Give the position of every leukocyte visible.
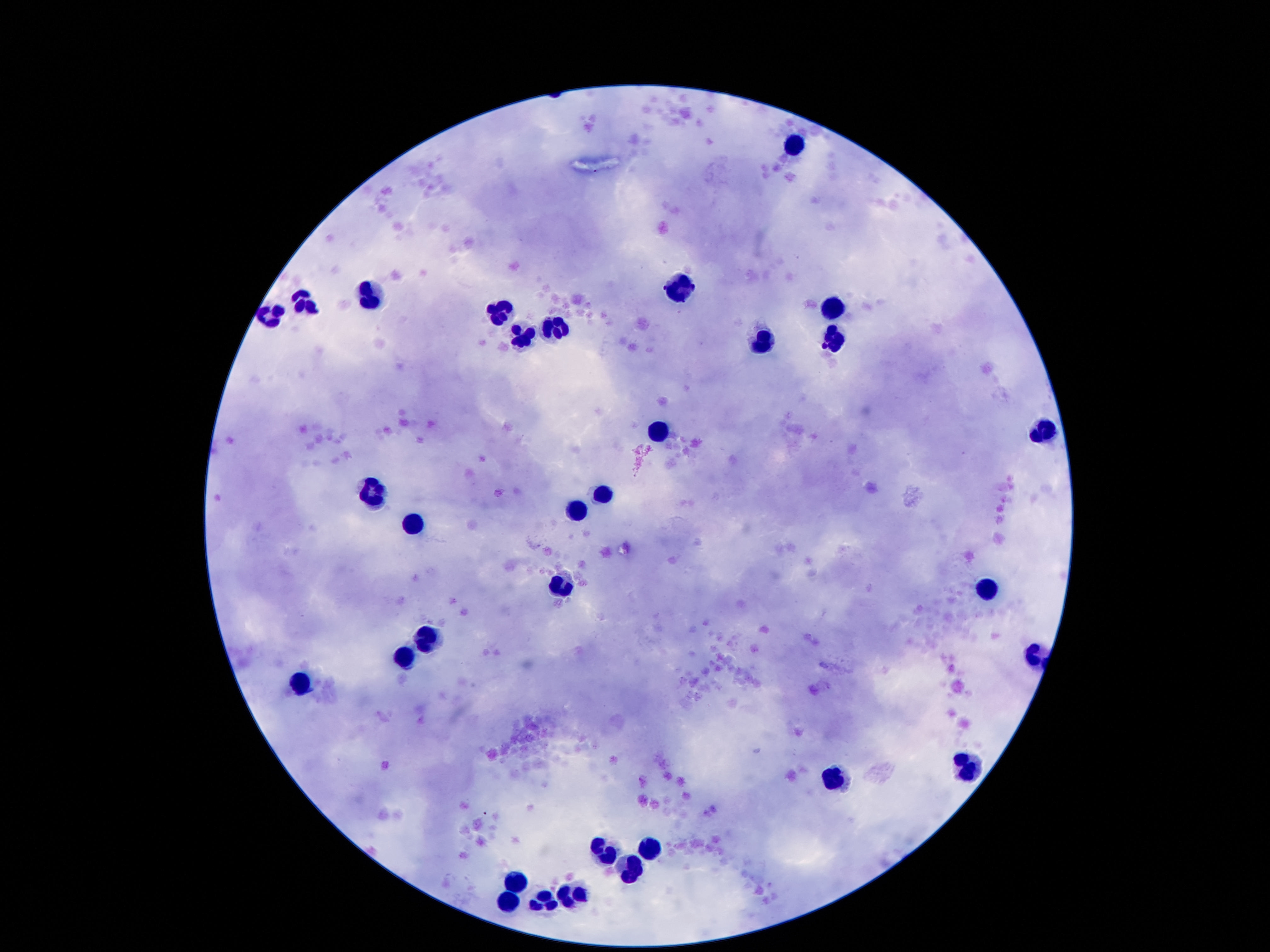

Approximate centers as (x, y) in pixels.
Leukocytes: (794, 145), (675, 288), (364, 297), (307, 303), (833, 305), (503, 311), (266, 317), (559, 323), (524, 335), (763, 340), (833, 340), (659, 428), (1040, 434), (604, 495), (374, 497), (577, 512), (413, 528), (563, 582), (987, 594), (428, 633), (401, 659), (303, 682), (968, 766), (839, 780), (651, 842), (602, 854), (634, 864), (516, 883), (579, 891), (509, 899), (552, 905).

100x magnification. Giemsa stain. Image is 1270×952 pixels. Single field of view. Photographed through the microscope eyepiece with a smartphone camera. Patient malaria status: uninfected. Thick blood film.